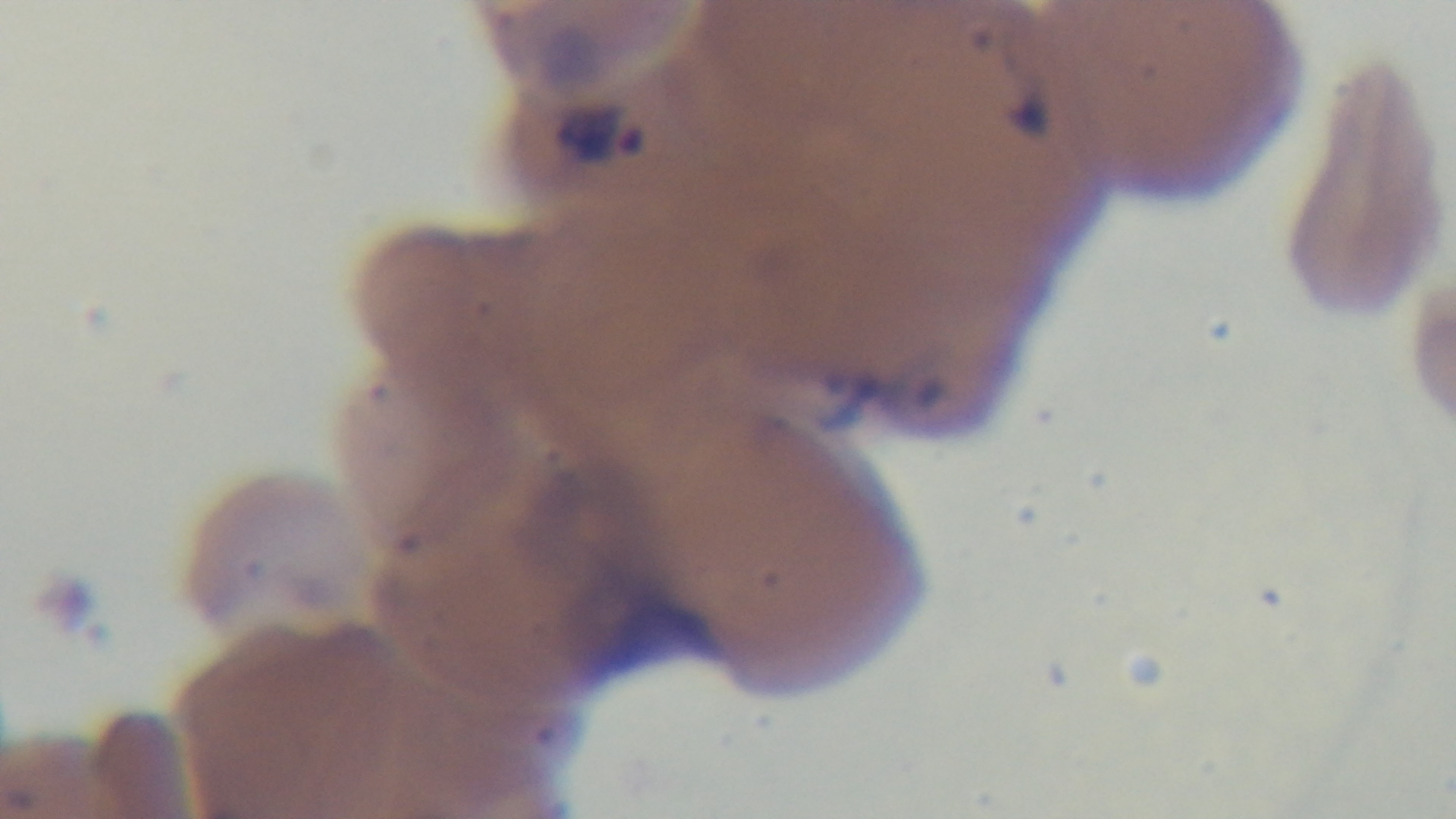
Malaria status: positive. 100x oil-immersion objective. Single field of view. Giemsa stain. Captured with a mounted 4K digital camera. Light microscopy. Preparation: thin smear.